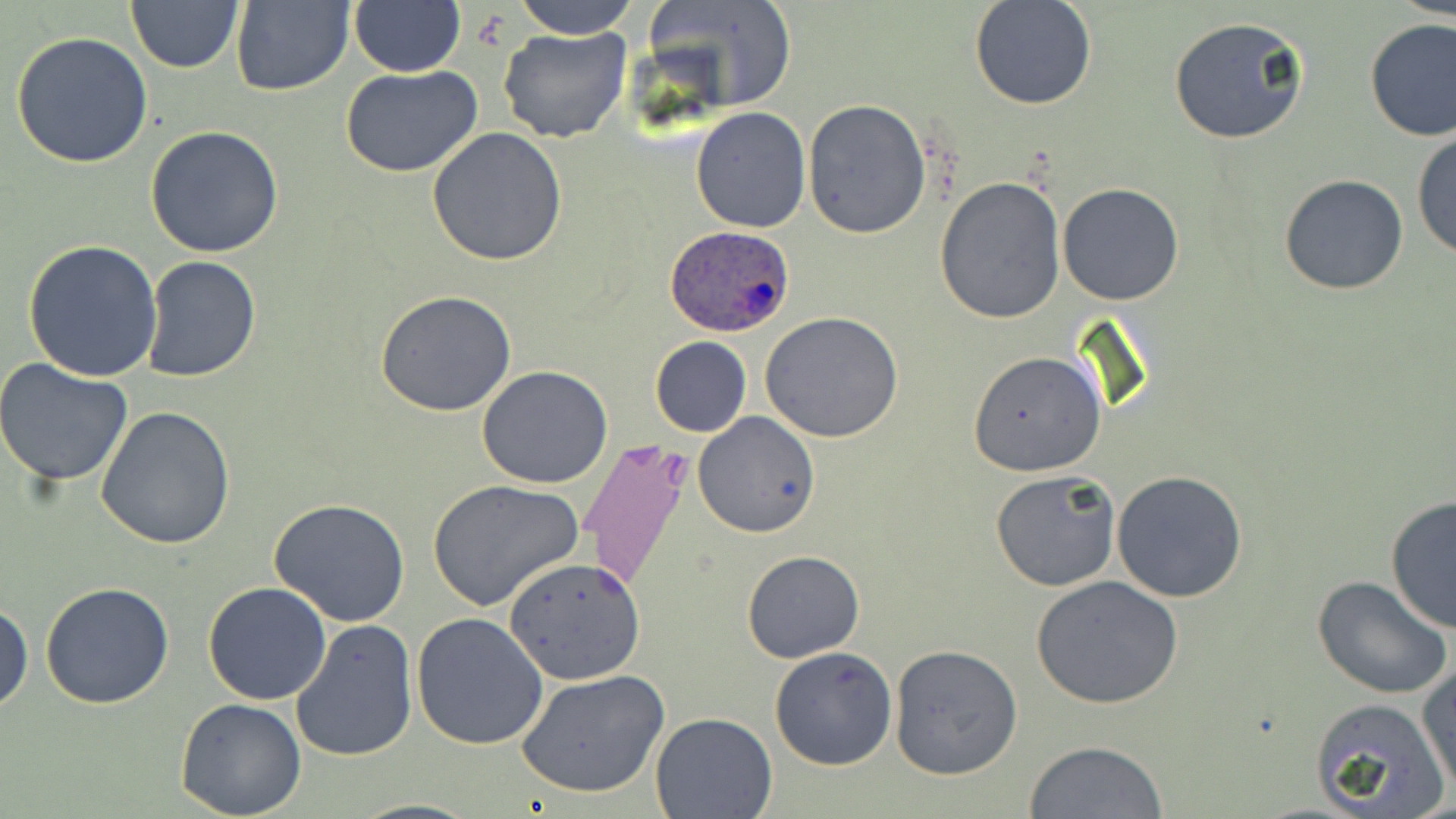
Summary:
  - Coordinate format: approximate bounding boxes as named x1/y1/x2/y2 corners in pixels
  - Plasmodium ovale-infected red blood cell locations: (x1=663, y1=225, x2=794, y2=337)
  - Uninfected red blood cell locations: (x1=509, y1=0, x2=641, y2=38), (x1=642, y1=0, x2=798, y2=110), (x1=969, y1=0, x2=1096, y2=110), (x1=125, y1=1, x2=243, y2=73), (x1=230, y1=1, x2=352, y2=96), (x1=348, y1=1, x2=466, y2=76), (x1=1168, y1=16, x2=1309, y2=144), (x1=1363, y1=18, x2=1456, y2=141), (x1=498, y1=26, x2=632, y2=143), (x1=10, y1=30, x2=154, y2=168), (x1=339, y1=66, x2=486, y2=179), (x1=802, y1=99, x2=932, y2=238), (x1=691, y1=107, x2=811, y2=232), (x1=145, y1=125, x2=284, y2=258), (x1=427, y1=129, x2=567, y2=267), (x1=1412, y1=130, x2=1456, y2=261), (x1=1278, y1=173, x2=1409, y2=296), (x1=933, y1=177, x2=1067, y2=325), (x1=1057, y1=182, x2=1185, y2=304), (x1=22, y1=239, x2=163, y2=383), (x1=140, y1=256, x2=262, y2=384), (x1=374, y1=289, x2=518, y2=415), (x1=760, y1=312, x2=904, y2=444), (x1=649, y1=337, x2=752, y2=438), (x1=968, y1=350, x2=1107, y2=477), (x1=0, y1=358, x2=133, y2=486), (x1=476, y1=365, x2=612, y2=489), (x1=95, y1=406, x2=236, y2=550), (x1=693, y1=411, x2=820, y2=538), (x1=989, y1=468, x2=1122, y2=593), (x1=1111, y1=470, x2=1248, y2=602), (x1=428, y1=480, x2=586, y2=615), (x1=1385, y1=495, x2=1456, y2=634), (x1=268, y1=497, x2=411, y2=627), (x1=740, y1=550, x2=865, y2=662), (x1=501, y1=554, x2=646, y2=685), (x1=1030, y1=575, x2=1183, y2=708), (x1=1312, y1=575, x2=1456, y2=701), (x1=40, y1=582, x2=176, y2=709), (x1=203, y1=582, x2=331, y2=704), (x1=0, y1=599, x2=33, y2=714), (x1=412, y1=612, x2=549, y2=749), (x1=292, y1=620, x2=419, y2=762), (x1=889, y1=644, x2=1023, y2=779), (x1=768, y1=645, x2=898, y2=771), (x1=1418, y1=661, x2=1455, y2=795), (x1=515, y1=669, x2=670, y2=799), (x1=1308, y1=698, x2=1448, y2=818), (x1=174, y1=699, x2=306, y2=818), (x1=650, y1=712, x2=778, y2=819), (x1=1023, y1=740, x2=1169, y2=818)
  - Slide-level diagnosis: Plasmodium ovale
  - Image size: 1456×819 pixels
  - Stain: May-Grünwald-Giemsa
  - Preparation: thin blood smear
  - Magnification: 1000x
  - Field of view: single
  - Modality: light microscopy